Identify the parasite.
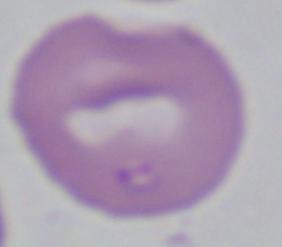

This is Babesia.

Summary:
  - Modality: micrograph
  - Magnification: 1000x